Classify this cell by malaria status.
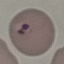
Parasitized.

capture = smartphone camera at the microscope eyepiece
preparation = thin blood smear
image type = cell patch, automatically extracted from a larger field of view and resized to 64 × 64 pixels
stain = Giemsa